Give the extent of all Plasmodium ovale-infected red blood cells.
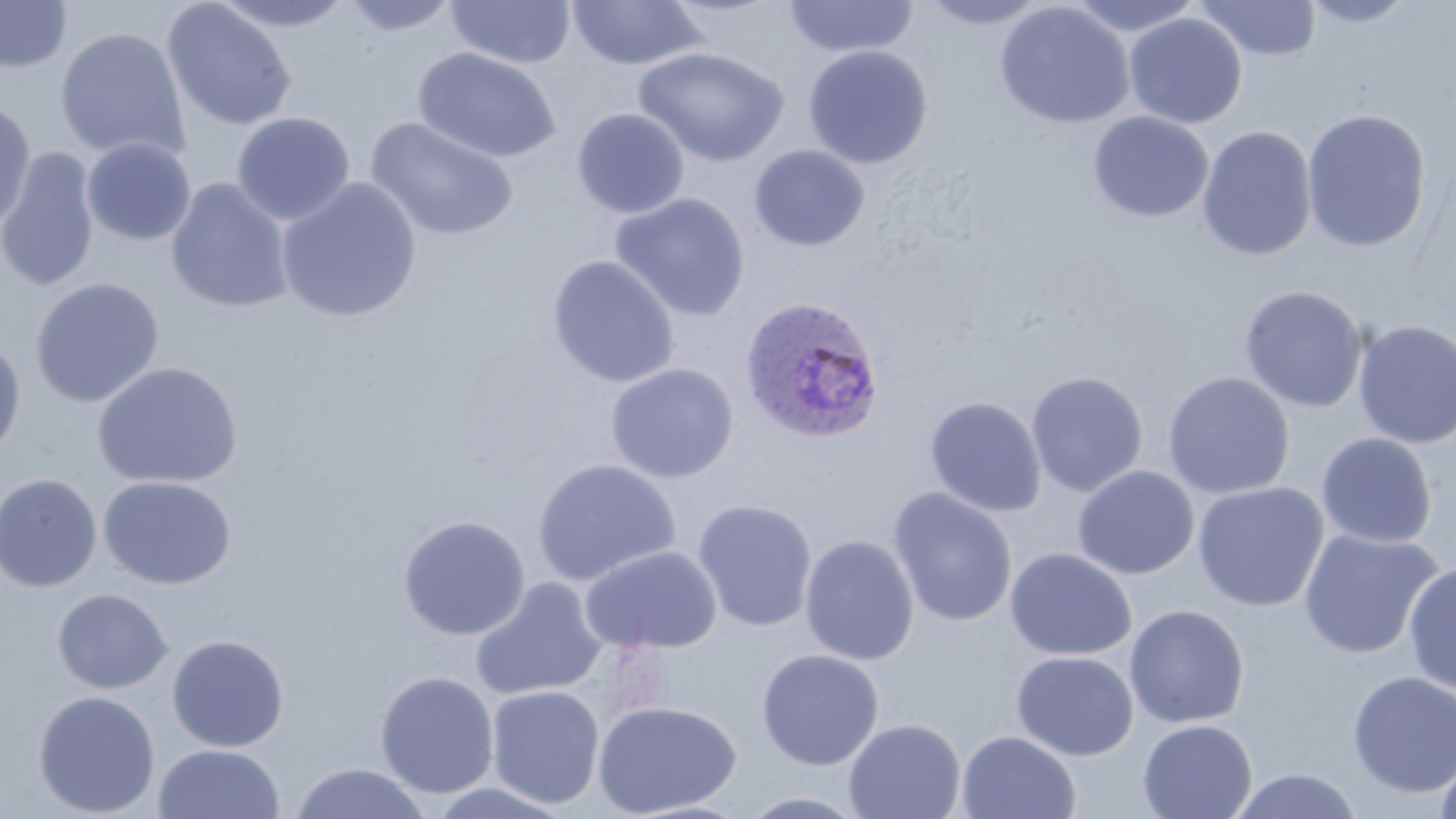
Approximate bounding boxes as (x1, y1, x2, y2) in pixels.
Plasmodium ovale-infected red blood cells: (738, 295, 886, 446).

Uninfected red blood cell locations: (0, 0, 73, 74), (338, 0, 463, 36), (566, 0, 707, 70), (782, 0, 919, 58), (917, 0, 1053, 29), (1065, 0, 1205, 37), (1193, 0, 1323, 62), (1298, 0, 1418, 28), (161, 1, 298, 132), (209, 1, 357, 32), (445, 1, 576, 69), (994, 2, 1134, 129), (1123, 12, 1248, 129), (54, 26, 191, 162), (802, 44, 934, 170), (633, 46, 790, 167), (412, 47, 561, 164), (0, 96, 36, 231), (571, 108, 690, 219), (1301, 108, 1432, 253), (231, 111, 355, 225), (1087, 111, 1214, 223), (365, 116, 519, 242), (1197, 124, 1318, 262), (81, 137, 196, 246), (748, 144, 871, 252), (0, 148, 100, 292), (277, 177, 423, 323), (166, 178, 294, 314), (610, 192, 751, 322), (546, 254, 680, 389), (30, 278, 165, 408), (1239, 285, 1369, 413), (1352, 319, 1456, 449), (0, 331, 26, 465), (91, 361, 244, 489), (604, 362, 740, 484), (1026, 370, 1149, 497), (1162, 371, 1295, 500), (924, 395, 1047, 517), (1315, 432, 1438, 549), (531, 458, 682, 588), (1072, 465, 1200, 580), (0, 473, 103, 592), (98, 476, 236, 589), (1192, 481, 1329, 612), (887, 486, 1018, 627), (691, 498, 818, 632), (397, 513, 531, 641), (1297, 528, 1444, 660), (799, 533, 919, 666), (580, 545, 723, 654), (1004, 547, 1138, 661), (1402, 561, 1456, 697), (471, 578, 607, 701), (52, 587, 174, 694), (1123, 604, 1249, 728), (167, 634, 289, 753), (756, 648, 884, 771), (1011, 651, 1139, 760), (374, 670, 499, 799), (1347, 670, 1456, 798), (486, 685, 605, 808), (33, 690, 160, 817), (592, 699, 742, 817), (842, 717, 966, 819), (1136, 718, 1258, 819), (956, 730, 1082, 819), (153, 743, 285, 818), (1432, 750, 1456, 819), (288, 762, 433, 819), (1229, 768, 1363, 819), (423, 781, 576, 819), (738, 790, 872, 818). Slide-level diagnosis: Plasmodium ovale. Optical microscopy. Image is 1456×819 pixels. May-Grünwald-Giemsa-stained preparation. One field of a larger specimen. Thin blood smear. 1000x magnification.